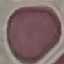 Malaria status: uninfected. Acquired by smartphone through the microscope eyepiece. Giemsa-stained preparation. Thin blood film. Cell patch, automatically extracted from a larger field of view and resized to 64 × 64 pixels.